Describe the morphology of the red blood cells.
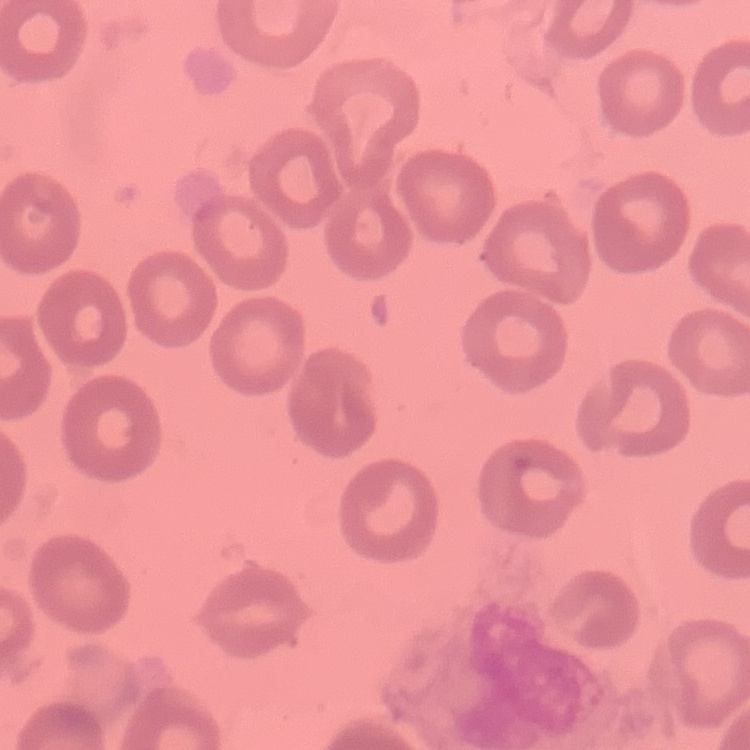
They show no rouleaux formation.

preparation = thin blood film
stain = Field's or Giemsa
image type = one tile cut from a larger photomicrograph